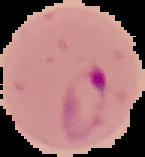
Image is 145×157 pixels. Result: Plasmodium parasites identified. From a thin blood smear. Segmented cell region on a black background.